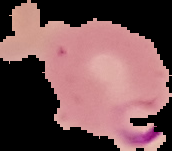
Result: Plasmodium parasites identified. Segmented cell region on a black background. Image is 172×151 pixels. From a thin blood film.